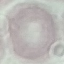

Summary:
  - Result: no malaria parasites seen
  - Image type: cell patch, automatically extracted from a larger field of view and resized to 64 × 64 pixels
  - Stain: Giemsa
  - Capture: smartphone camera at the microscope eyepiece
  - Preparation: thin blood film